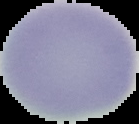

{
  "preparation": "thin blood smear",
  "image_size": "139×124 pixels",
  "result": "no malaria parasites detected",
  "image_type": "segmented cell region with the area outside set to black"
}